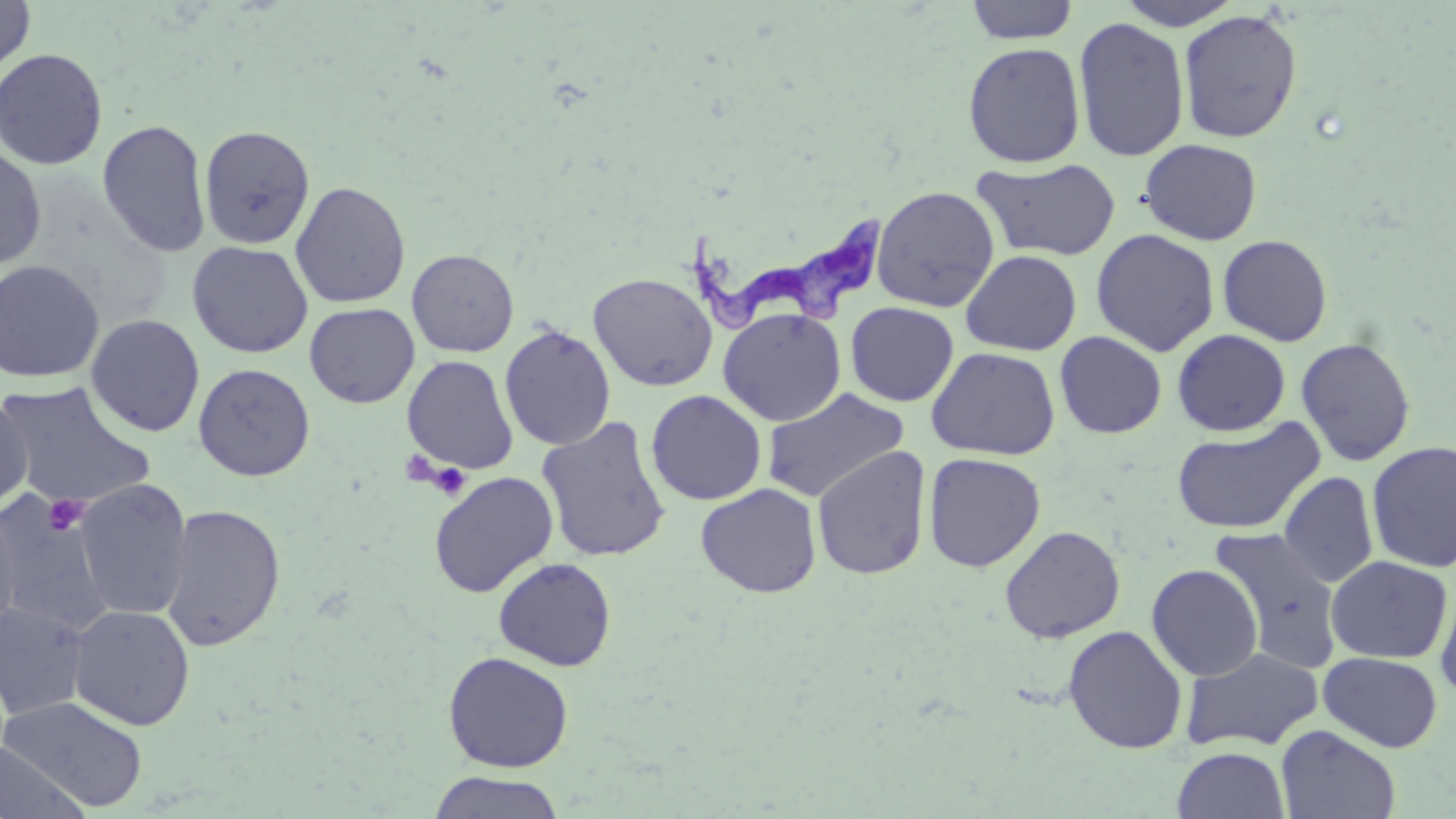
slide-level diagnosis = Trypanosoma brucei
magnification = 1000x
modality = optical microscopy
stain = May-Grünwald-Giemsa
image size = 1456×819 pixels
preparation = thin blood film
platelet locations = approximate bounding boxes as named x1/y1/x2/y2 corners in pixels: (x1=427, y1=462, x2=471, y2=499), (x1=43, y1=493, x2=89, y2=536)
field of view = single
uninfected red blood cell locations = approximate bounding boxes as named x1/y1/x2/y2 corners in pixels: (x1=0, y1=0, x2=35, y2=76), (x1=1114, y1=0, x2=1245, y2=29), (x1=965, y1=1, x2=1079, y2=44), (x1=1178, y1=9, x2=1303, y2=143), (x1=1073, y1=16, x2=1190, y2=162), (x1=962, y1=42, x2=1086, y2=168), (x1=0, y1=48, x2=108, y2=170), (x1=97, y1=119, x2=212, y2=257), (x1=198, y1=124, x2=316, y2=250), (x1=1139, y1=138, x2=1262, y2=245), (x1=0, y1=145, x2=46, y2=271), (x1=974, y1=157, x2=1121, y2=261), (x1=290, y1=181, x2=411, y2=308), (x1=871, y1=186, x2=1000, y2=313), (x1=1091, y1=229, x2=1219, y2=356), (x1=1218, y1=234, x2=1333, y2=347), (x1=187, y1=241, x2=314, y2=359), (x1=406, y1=249, x2=519, y2=357), (x1=961, y1=250, x2=1082, y2=356), (x1=0, y1=259, x2=105, y2=383), (x1=588, y1=272, x2=718, y2=391), (x1=845, y1=302, x2=959, y2=406), (x1=304, y1=303, x2=419, y2=408), (x1=718, y1=307, x2=846, y2=427), (x1=85, y1=313, x2=205, y2=437), (x1=500, y1=325, x2=616, y2=451), (x1=1172, y1=329, x2=1291, y2=436), (x1=1054, y1=331, x2=1167, y2=439), (x1=1296, y1=337, x2=1416, y2=467), (x1=926, y1=346, x2=1061, y2=461), (x1=402, y1=354, x2=518, y2=474), (x1=193, y1=363, x2=315, y2=482), (x1=0, y1=380, x2=156, y2=510), (x1=762, y1=387, x2=909, y2=504), (x1=646, y1=390, x2=767, y2=505), (x1=0, y1=394, x2=33, y2=513), (x1=536, y1=416, x2=671, y2=562), (x1=1172, y1=419, x2=1325, y2=535), (x1=1366, y1=440, x2=1456, y2=573), (x1=812, y1=446, x2=932, y2=580), (x1=923, y1=452, x2=1046, y2=572), (x1=428, y1=472, x2=559, y2=598), (x1=1279, y1=472, x2=1378, y2=588), (x1=74, y1=479, x2=192, y2=621), (x1=695, y1=483, x2=822, y2=598), (x1=0, y1=498, x2=116, y2=635), (x1=160, y1=504, x2=286, y2=652), (x1=0, y1=506, x2=21, y2=643), (x1=1000, y1=526, x2=1126, y2=644), (x1=1208, y1=527, x2=1345, y2=672), (x1=1325, y1=555, x2=1453, y2=663), (x1=493, y1=557, x2=617, y2=671), (x1=1146, y1=564, x2=1264, y2=681), (x1=1435, y1=583, x2=1456, y2=703), (x1=0, y1=600, x2=92, y2=720), (x1=67, y1=604, x2=195, y2=730), (x1=1063, y1=625, x2=1188, y2=754), (x1=1181, y1=646, x2=1324, y2=752), (x1=442, y1=651, x2=574, y2=773), (x1=1319, y1=652, x2=1443, y2=752), (x1=1, y1=695, x2=148, y2=812), (x1=1276, y1=725, x2=1400, y2=819), (x1=0, y1=741, x2=89, y2=819), (x1=1172, y1=746, x2=1290, y2=819), (x1=428, y1=771, x2=565, y2=819)
Trypanosoma brucei locations = approximate bounding boxes as named x1/y1/x2/y2 corners in pixels: (x1=686, y1=217, x2=885, y2=332)